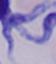

Summary:
  - Modality: photomicrograph
  - Magnification: 1000x
  - Identification: trypanosome